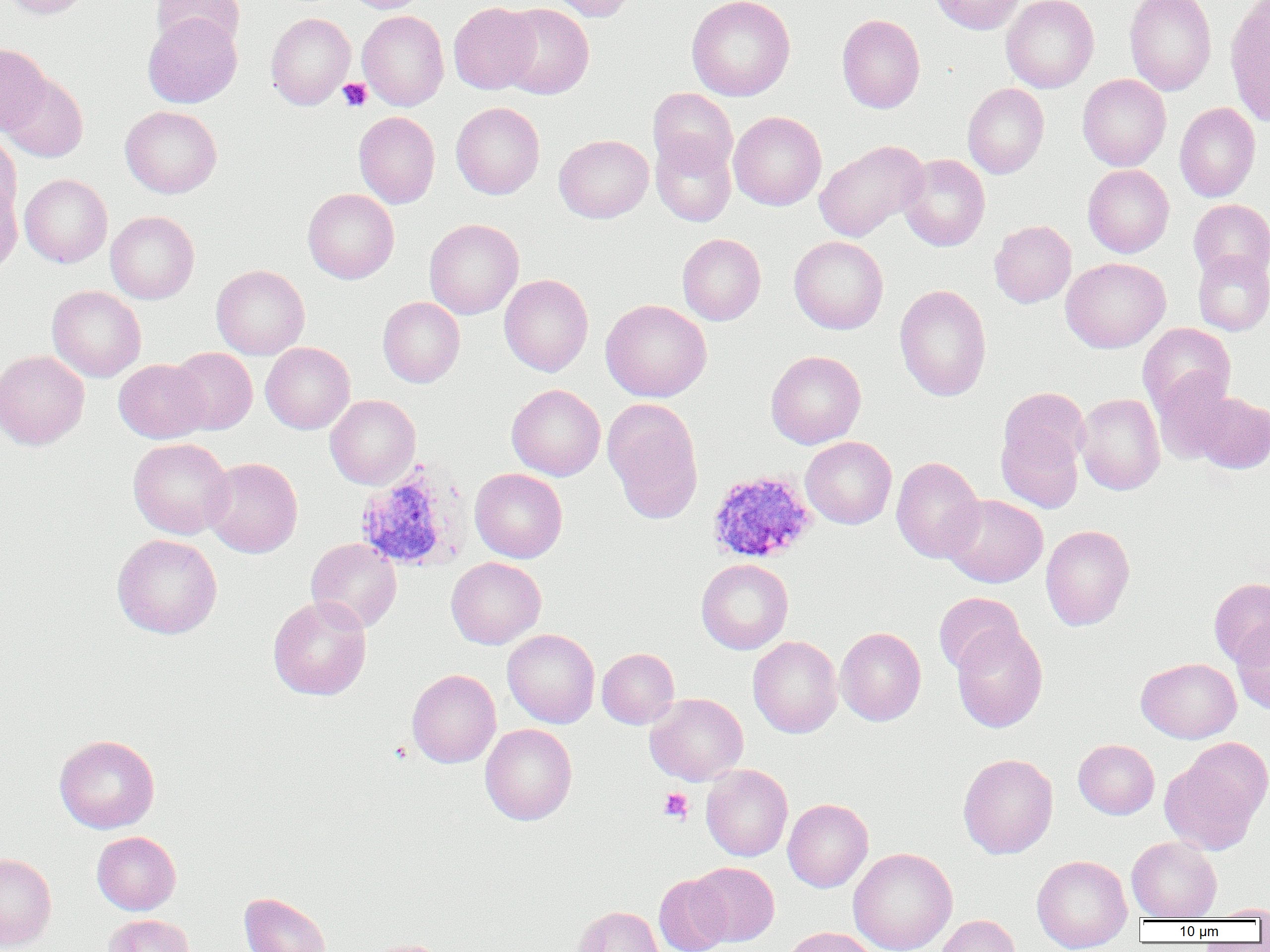

slide-level diagnosis = Plasmodium ovale
image size = 1270×952 pixels
modality = light microscopy
Plasmodium ovale-infected red blood cell locations = approximate bounding boxes as [x1, y1, x2, y2] in pixels: [358, 461, 476, 573], [709, 472, 819, 566]
preparation = thin blood smear
uninfected red blood cell locations = approximate bounding boxes as [x1, y1, x2, y2] in pixels: [2, 0, 91, 19], [342, 0, 430, 13], [547, 0, 639, 22], [686, 0, 796, 101], [929, 0, 1026, 34], [1001, 0, 1099, 93], [1124, 0, 1216, 95], [151, 1, 244, 52], [1224, 1, 1270, 128], [448, 2, 540, 94], [498, 3, 594, 99], [357, 11, 449, 111], [265, 13, 355, 109], [143, 14, 242, 107], [836, 14, 925, 113], [0, 42, 52, 135], [2, 71, 88, 162], [1077, 74, 1170, 171], [962, 83, 1049, 178], [647, 88, 738, 176], [451, 102, 545, 199], [1174, 102, 1260, 202], [120, 106, 222, 198], [353, 111, 440, 208], [728, 111, 827, 210], [0, 133, 21, 220], [554, 134, 653, 223], [651, 134, 736, 227], [814, 140, 928, 241], [898, 154, 990, 251], [1082, 165, 1174, 257], [20, 174, 112, 268], [0, 179, 23, 277], [303, 188, 399, 283], [1188, 199, 1270, 282], [105, 211, 199, 304], [424, 219, 523, 319], [989, 220, 1076, 308], [677, 233, 766, 325], [789, 236, 888, 334], [1193, 250, 1270, 335], [1060, 257, 1170, 353], [211, 264, 310, 359], [499, 274, 593, 376], [47, 285, 146, 382], [894, 285, 992, 401], [378, 297, 465, 387], [600, 299, 712, 402], [1137, 323, 1236, 416], [260, 342, 355, 434], [169, 348, 257, 435], [0, 350, 89, 450], [766, 351, 866, 449], [114, 359, 211, 443], [1152, 372, 1239, 465], [506, 384, 605, 480], [998, 387, 1090, 473], [1193, 392, 1270, 473], [1075, 393, 1165, 495], [325, 395, 420, 489], [602, 398, 704, 525], [996, 419, 1085, 513], [800, 437, 897, 529], [129, 438, 234, 539], [891, 456, 985, 564], [203, 457, 303, 558], [469, 468, 568, 563], [943, 494, 1047, 588], [1041, 524, 1135, 631], [112, 534, 222, 639], [306, 538, 402, 633], [446, 557, 546, 649], [696, 558, 793, 654], [1209, 577, 1270, 667], [933, 592, 1025, 676], [268, 595, 372, 701], [1231, 620, 1270, 714], [950, 623, 1048, 733], [835, 627, 926, 726], [503, 628, 600, 728], [747, 636, 842, 738], [597, 648, 679, 729], [1136, 658, 1241, 743], [407, 669, 501, 768], [645, 693, 748, 786], [480, 723, 577, 825], [54, 734, 160, 833], [1183, 736, 1269, 822], [1073, 739, 1159, 819], [957, 753, 1058, 859], [1160, 756, 1263, 854], [701, 764, 792, 861], [783, 798, 873, 892], [91, 831, 181, 915], [1126, 836, 1222, 920], [848, 848, 957, 952], [0, 852, 56, 951], [1032, 855, 1132, 952], [689, 862, 779, 946], [654, 874, 732, 952], [239, 892, 330, 952], [1206, 903, 1270, 920], [573, 905, 664, 952], [103, 914, 195, 952], [934, 914, 1020, 952], [782, 927, 877, 952], [365, 939, 450, 952]
field of view = single
platelet locations = approximate bounding boxes as [x1, y1, x2, y2] in pixels: [337, 78, 372, 112], [658, 788, 693, 824]
magnification = 1000x